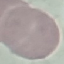

Summary:
  - Result: negative for malaria parasites
  - Preparation: thin blood smear
  - Stain: Giemsa
  - Image type: automatically extracted cell patch, resized to 64 × 64 pixels
  - Capture: smartphone through the microscope eyepiece